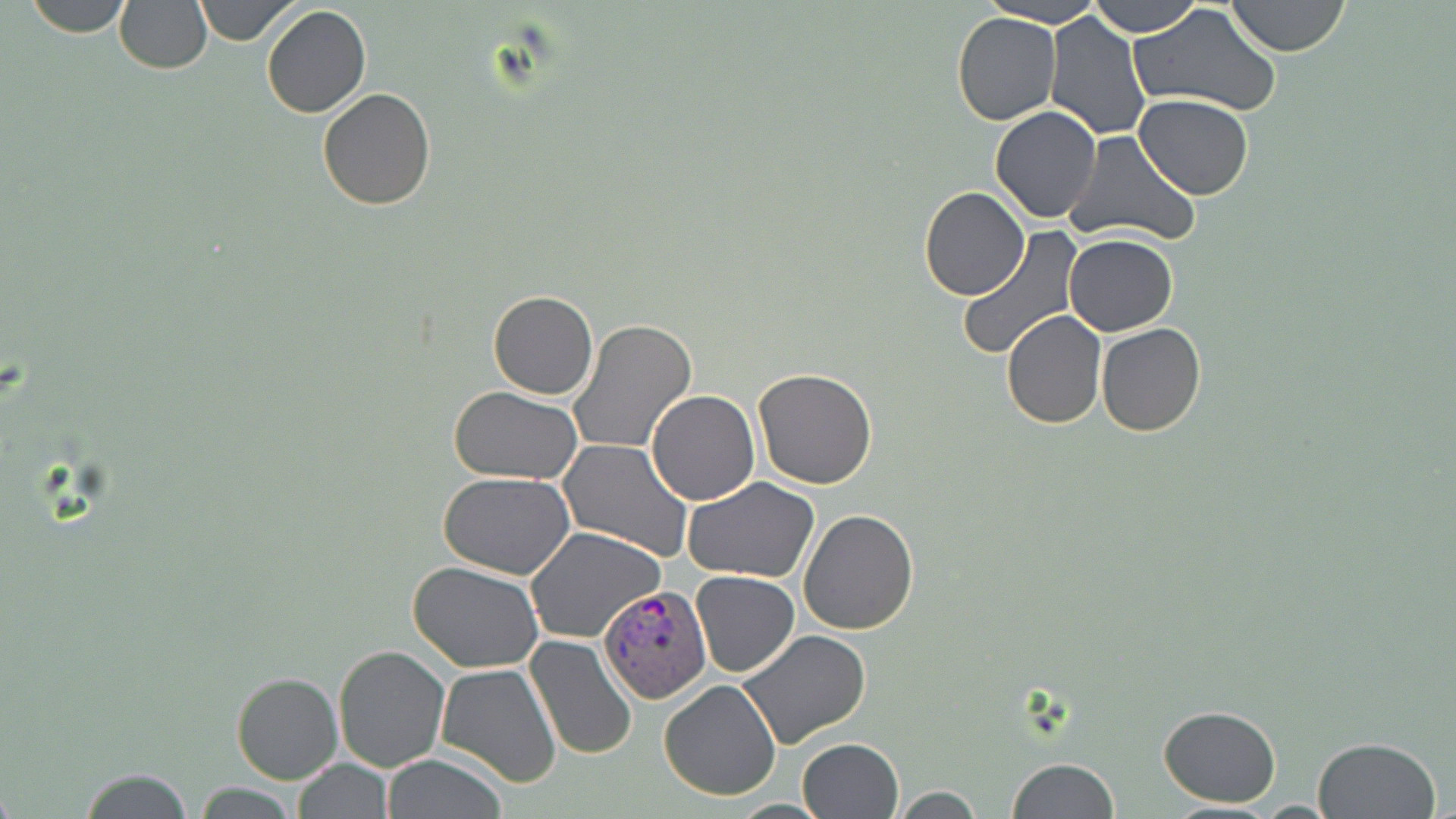

Summary:
  - Coordinate format: approximate bounding boxes as named x1/y1/x2/y2 corners in pixels
  - Plasmodium vivax-infected red blood cell locations: (x1=598, y1=584, x2=713, y2=704)
  - Uninfected red blood cell locations: (x1=21, y1=0, x2=134, y2=37), (x1=113, y1=0, x2=212, y2=73), (x1=193, y1=0, x2=299, y2=46), (x1=1089, y1=0, x2=1201, y2=37), (x1=1226, y1=0, x2=1349, y2=57), (x1=981, y1=2, x2=1106, y2=26), (x1=1129, y1=3, x2=1283, y2=119), (x1=260, y1=4, x2=371, y2=118), (x1=1044, y1=11, x2=1152, y2=140), (x1=951, y1=13, x2=1062, y2=125), (x1=317, y1=87, x2=436, y2=210), (x1=1134, y1=94, x2=1254, y2=200), (x1=990, y1=106, x2=1102, y2=223), (x1=1062, y1=129, x2=1199, y2=249), (x1=919, y1=185, x2=1030, y2=301), (x1=955, y1=229, x2=1080, y2=361), (x1=1064, y1=235, x2=1178, y2=336), (x1=487, y1=290, x2=597, y2=400), (x1=1000, y1=309, x2=1107, y2=428), (x1=569, y1=318, x2=697, y2=455), (x1=1096, y1=323, x2=1207, y2=436), (x1=751, y1=368, x2=879, y2=488), (x1=448, y1=386, x2=584, y2=485), (x1=646, y1=390, x2=760, y2=506), (x1=559, y1=438, x2=694, y2=561), (x1=438, y1=471, x2=575, y2=577), (x1=682, y1=477, x2=821, y2=581), (x1=798, y1=509, x2=919, y2=634), (x1=525, y1=528, x2=665, y2=644), (x1=409, y1=561, x2=545, y2=673), (x1=692, y1=571, x2=801, y2=677), (x1=738, y1=629, x2=873, y2=752), (x1=524, y1=634, x2=639, y2=761), (x1=333, y1=645, x2=450, y2=771), (x1=434, y1=664, x2=563, y2=788), (x1=230, y1=672, x2=343, y2=785), (x1=659, y1=680, x2=782, y2=802), (x1=1159, y1=706, x2=1281, y2=807), (x1=1311, y1=736, x2=1441, y2=819), (x1=796, y1=737, x2=904, y2=819), (x1=381, y1=754, x2=509, y2=818), (x1=291, y1=757, x2=392, y2=818), (x1=1007, y1=758, x2=1121, y2=819), (x1=75, y1=768, x2=195, y2=818), (x1=189, y1=783, x2=303, y2=818), (x1=891, y1=786, x2=987, y2=818), (x1=1153, y1=801, x2=1290, y2=818)
  - Slide-level diagnosis: Plasmodium vivax
  - Magnification: 1000x
  - Preparation: thin blood smear
  - Stain: May-Grünwald-Giemsa
  - Field of view: one of a larger specimen
  - Image size: 1456×819 pixels
  - Modality: optical microscopy